Report the malaria status of this cell.
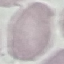
It is uninfected.

image type = cell patch, automatically extracted from a larger field of view and resized to 64 × 64 pixels
capture = smartphone camera at the microscope eyepiece
stain = Giemsa
preparation = thin blood smear